Assess this cell for malaria.
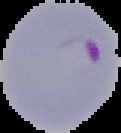

Parasitized.

From a thin blood film. The area outside the segmented cell region is set to black. Image is 121×133 pixels.